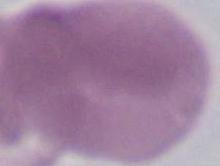 Captured at 1000x magnification. A red blood cell is shown. Photomicrograph.